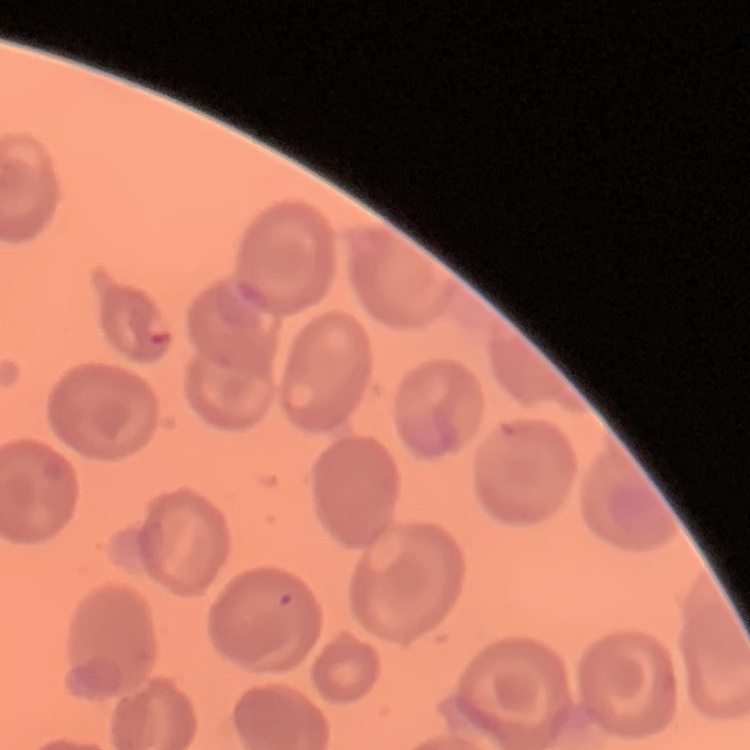
Summary:
  - Erythrocyte morphology: no rouleaux formation
  - Stain: Field's or Giemsa
  - Image type: square crop of a larger photomicrograph
  - Preparation: thin blood smear